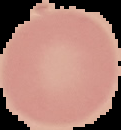
image_type: segmented cell region on a black background
preparation: thin blood smear
malaria_status: uninfected
image_size: 121×130 pixels